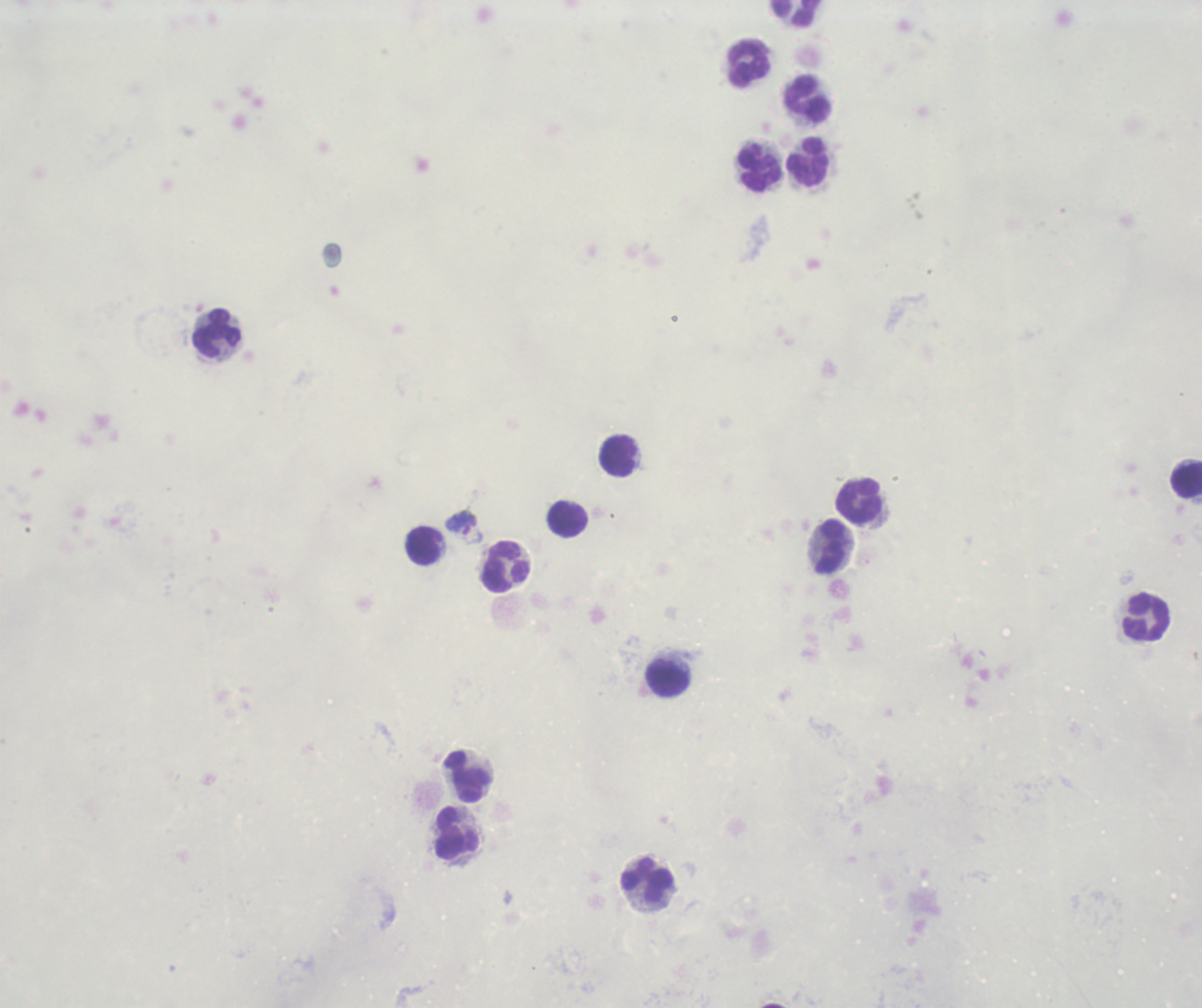
Approximate centers as (x, y) in pixels. Leukocyte locations: (798, 14), (750, 65), (808, 99), (809, 164), (761, 169), (218, 334), (619, 456), (1187, 480), (861, 502), (568, 521), (424, 545), (832, 548), (506, 568), (1147, 619), (669, 680), (469, 778), (458, 833), (648, 881). Gametocyte locations: (464, 527). One field from this slide. Previously used in a real diagnosis. Romanowsky-stained preparation. Thick blood smear. Image is 1202×1008 pixels. Result: Plasmodium parasites detected. 100x magnification. Background quality: poor.